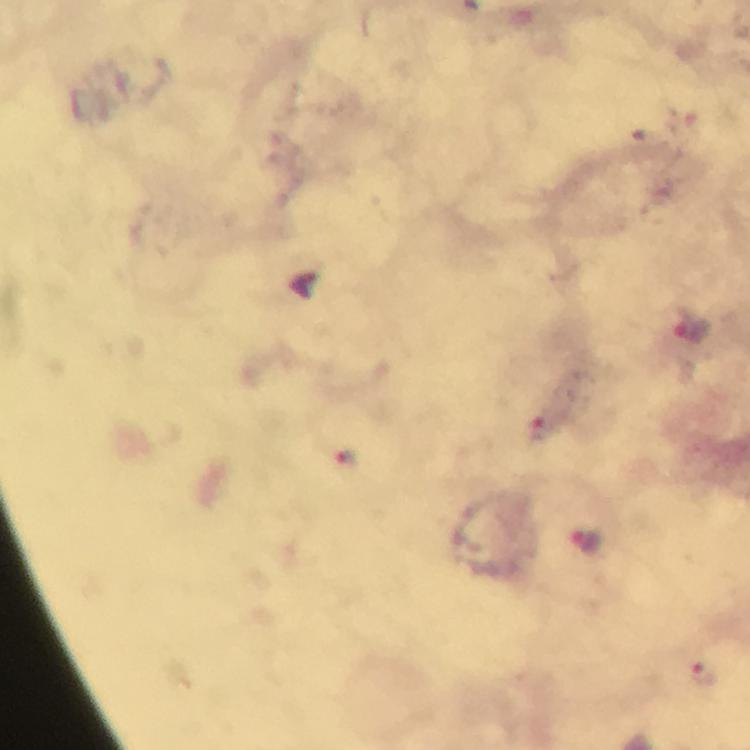
Approximate object centers, in pixels from the top-left corner.
Summary:
  - Plasmodium parasite locations: (x=308, y=289), (x=693, y=327), (x=587, y=539), (x=703, y=672)
  - Image size: 750×750 pixels
  - Preparation: thick blood film
  - Cropped from: one field of view
  - Magnification: 100x
  - Capture: smartphone mounted on the microscope
  - Immersion oil: used
  - Stain: Giemsa
  - Context: from a malaria diagnostic workup